Classify the preparation.
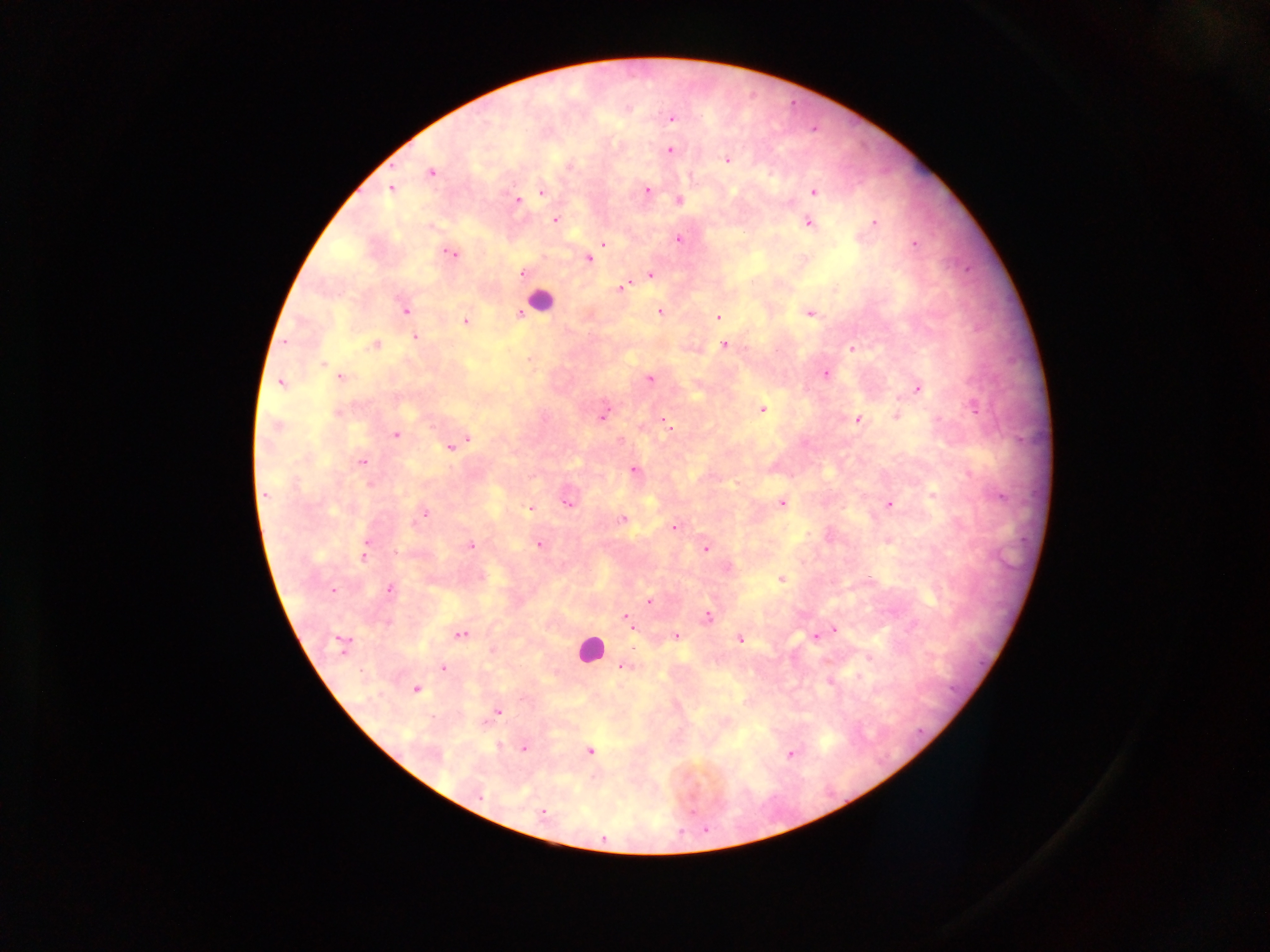

This is a thick smear.

{
  "field_of_view": "single",
  "country": "Ghana",
  "capture": "mobile-phone photograph through a microscope",
  "leukocyte_locations": "approximate centers as (x, y) in pixels: (540, 302), (589, 648)",
  "image_size": "1270×952 pixels",
  "malaria_parasite_locations": "approximate centers as (x, y) in pixels: (672, 119), (671, 150), (727, 160), (570, 166), (431, 173), (391, 190), (648, 190), (541, 191), (813, 192), (517, 200), (679, 200), (555, 220), (875, 222), (809, 224), (678, 239), (603, 243), (915, 244), (451, 253), (588, 259), (523, 273), (650, 276), (620, 288), (405, 309), (659, 311), (520, 314), (809, 314), (717, 317), (465, 322), (415, 337), (285, 342), (375, 345), (724, 345), (852, 348), (323, 365), (826, 373), (340, 378), (650, 379), (280, 382), (918, 388), (974, 407), (762, 409), (338, 412), (603, 416), (896, 417), (857, 420), (276, 426), (668, 427), (396, 435), (467, 438), (450, 447), (362, 461), (634, 469), (370, 484), (264, 494), (933, 495), (999, 497), (567, 503), (781, 504), (889, 505), (530, 508), (424, 513), (622, 520), (674, 527), (539, 545), (470, 546), (705, 548), (397, 552), (364, 556), (781, 578), (389, 589), (333, 590), (650, 601), (707, 617), (628, 619), (386, 623), (632, 625), (835, 629), (461, 634), (676, 636), (815, 636), (740, 640), (342, 643), (869, 658), (623, 667), (443, 668), (859, 676), (829, 682), (415, 689), (498, 711), (498, 746), (525, 748), (590, 751), (790, 753), (479, 794), (542, 811), (705, 830)"
}